Name the cell type shown.
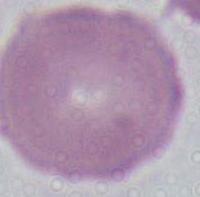
An erythrocyte.

Micrograph. 1000x magnification.